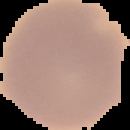
{
  "result": "no malaria parasites seen",
  "preparation": "thin blood smear",
  "image_type": "cell region segmented out of the field of view; surrounding area masked to black",
  "image_size": "130×130 pixels"
}